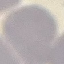
result: no malaria parasites seen
capture: smartphone through the microscope eyepiece
stain: Giemsa
image_type: cell patch, automatically extracted from a larger field of view and resized to 64 × 64 pixels
preparation: thin smear